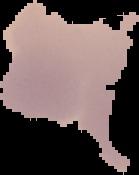
image_size: 139×175 pixels
preparation: thin blood smear
image_type: segmented cell region with the area outside set to black
malaria_status: uninfected